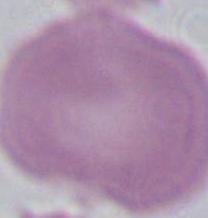

Summary:
  - Modality: micrograph
  - Magnification: 1000x
  - Identification: red blood cell